Locate every malaria parasite.
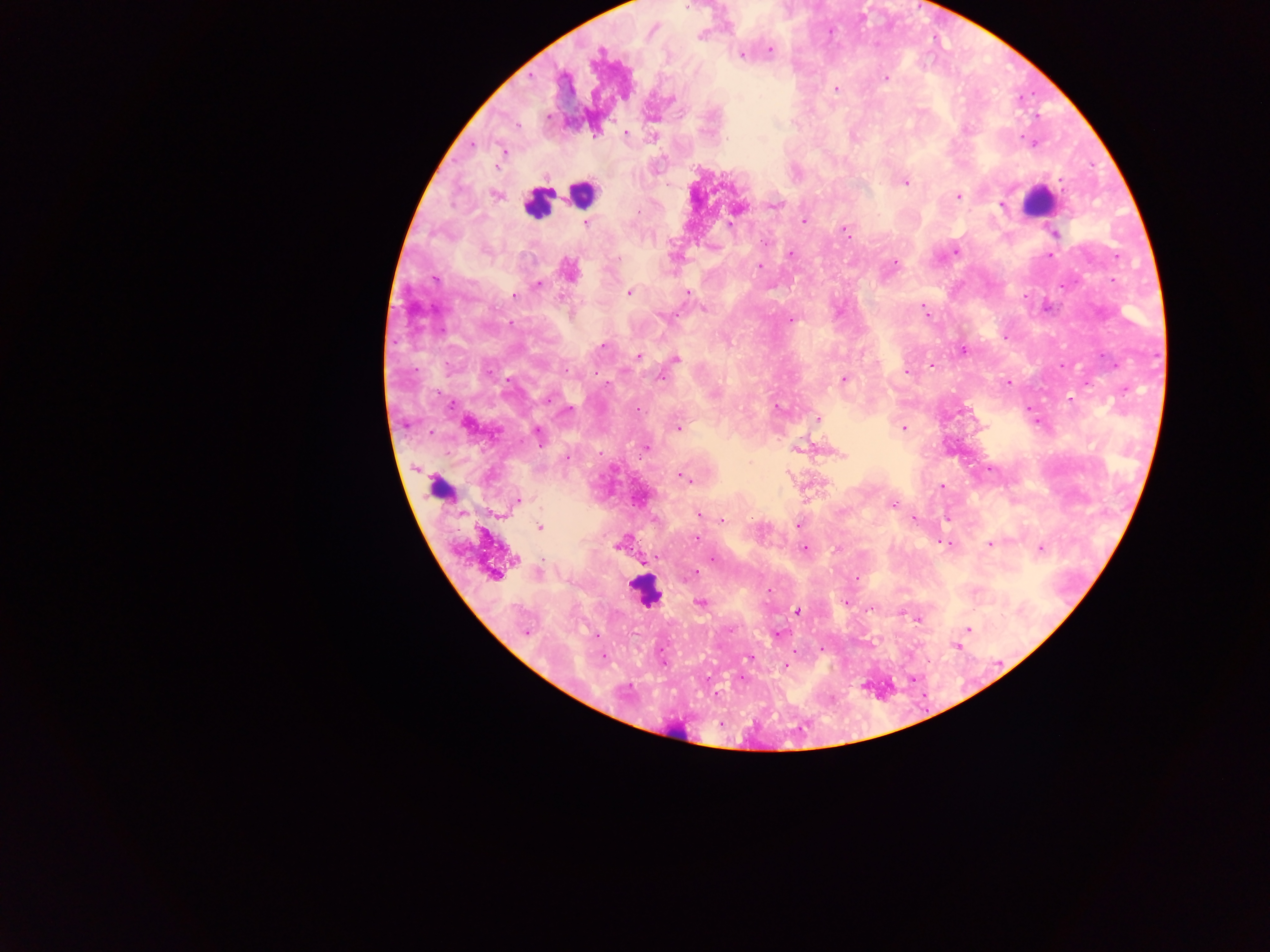
Approximate centers as {x, y} in pixels.
Malaria parasites: {700, 36}, {770, 50}, {599, 53}, {741, 55}, {886, 78}, {836, 88}, {966, 128}, {625, 133}, {726, 140}, {504, 151}, {906, 182}, {1061, 182}, {496, 195}, {958, 196}, {775, 205}, {1002, 205}, {638, 211}, {804, 221}, {586, 223}, {730, 225}, {846, 231}, {1055, 234}, {764, 243}, {485, 251}, {955, 252}, {791, 254}, {1051, 255}, {895, 263}, {760, 267}, {568, 270}, {434, 279}, {1062, 284}, {538, 285}, {629, 292}, {688, 292}, {514, 295}, {704, 308}, {924, 310}, {663, 317}, {791, 320}, {602, 346}, {963, 350}, {638, 356}, {675, 358}, {930, 365}, {1062, 366}, {907, 371}, {661, 377}, {844, 379}, {1009, 382}, {1088, 384}, {549, 398}, {777, 409}, {637, 410}, {568, 411}, {818, 419}, {467, 425}, {678, 428}, {903, 428}, {538, 433}, {646, 447}, {567, 458}, {684, 477}, {942, 486}, {518, 501}, {893, 505}, {699, 515}, {914, 519}, {723, 521}, {797, 524}, {539, 527}, {697, 539}, {990, 544}, {619, 545}, {944, 545}, {804, 548}, {1041, 548}, {713, 559}, {514, 560}, {694, 573}, {494, 574}, {768, 590}, {700, 603}, {845, 603}, {871, 609}, {797, 611}, {917, 619}, {968, 628}, {525, 633}, {777, 634}, {956, 645}, {603, 658}, {749, 658}, {664, 664}, {786, 665}.

Summary:
  - Leukocyte locations: {581, 194}, {1036, 201}, {536, 203}, {440, 489}, {645, 591}, {675, 734}
  - Country: Ghana
  - Capture: mobile-phone photograph through a microscope
  - Image size: 1270×952 pixels
  - Field of view: single
  - Preparation: thick blood smear